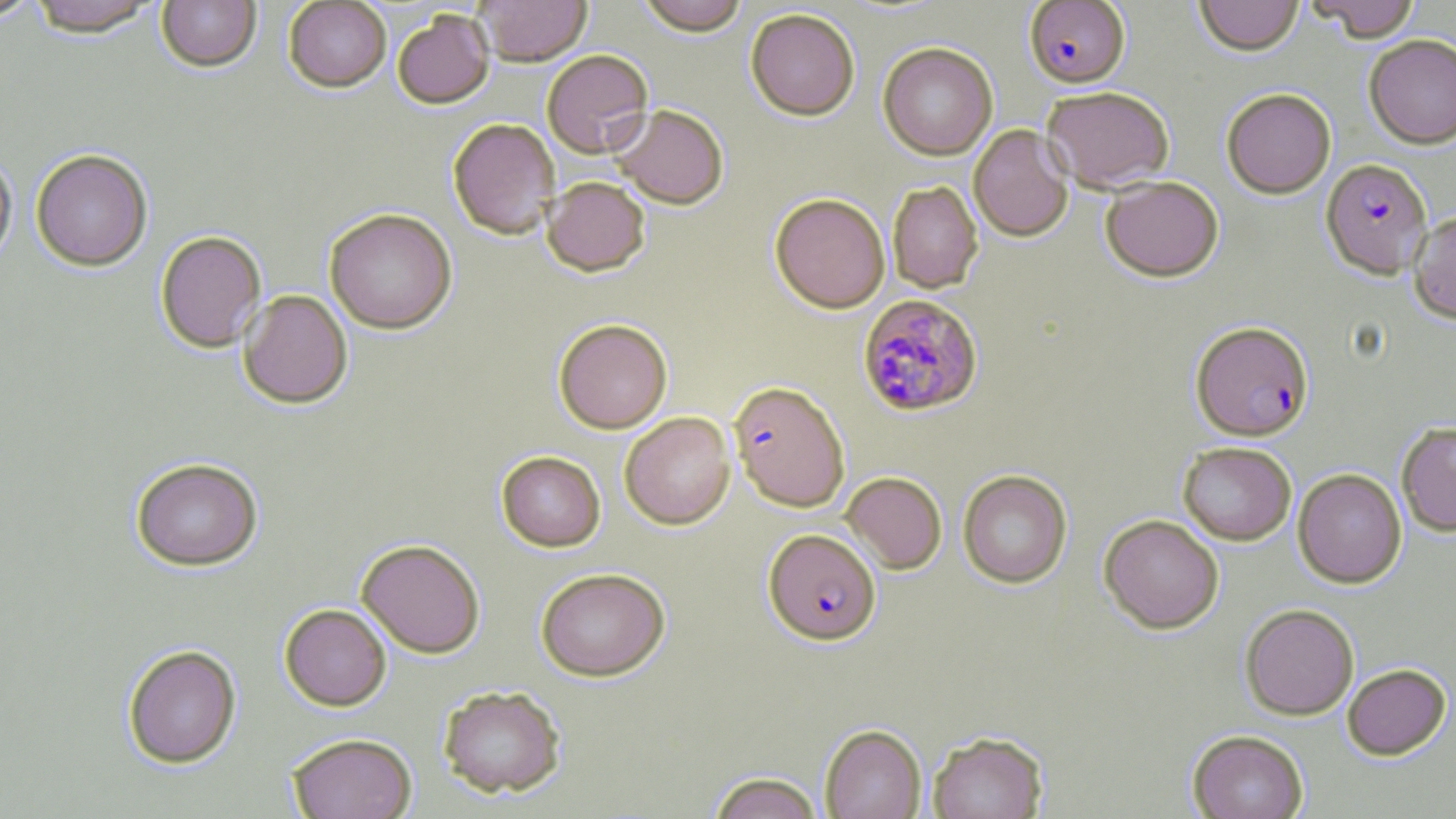
Summary:
  - Coordinate format: approximate bounding boxes as (x1,y1)-(x2,y2) corner pairs in pixels
  - Uninfected red blood cell locations: (0,0)-(44,23), (28,0)-(160,40), (156,0)-(261,75), (283,0)-(391,94), (475,0)-(592,68), (636,0)-(749,38), (1194,0)-(1304,58), (1308,0)-(1421,44), (746,10)-(860,122), (393,11)-(495,111), (1364,35)-(1456,149), (878,43)-(997,160), (542,51)-(654,160), (1042,87)-(1174,193), (1222,89)-(1336,199), (610,106)-(728,210), (448,119)-(560,240), (968,125)-(1074,242), (31,150)-(153,272), (0,151)-(17,268), (541,177)-(650,278), (1101,177)-(1224,283), (887,181)-(983,293), (770,194)-(890,313), (324,209)-(457,335), (1408,211)-(1456,323), (155,232)-(267,353), (238,291)-(352,410), (553,319)-(672,434), (620,412)-(735,530), (1396,421)-(1456,536), (1177,442)-(1296,546), (496,451)-(606,552), (130,458)-(264,573), (1293,469)-(1406,589), (958,470)-(1072,588), (841,472)-(947,574), (1099,515)-(1224,634), (356,539)-(485,658), (535,568)-(670,682), (279,604)-(392,711), (1240,604)-(1359,721), (122,645)-(242,769), (1342,665)-(1451,762), (437,685)-(566,799), (820,725)-(926,819), (927,730)-(1049,819), (1187,731)-(1308,819), (287,733)-(417,819), (707,771)-(825,819)
  - Plasmodium falciparum-infected red blood cell locations: (1024,1)-(1130,89), (1320,159)-(1433,279), (857,294)-(983,417), (1191,322)-(1313,441), (729,382)-(849,512), (763,530)-(881,646)
  - Slide-level diagnosis: Plasmodium falciparum
  - Image size: 1456×819 pixels
  - Field of view: single
  - Preparation: thin blood smear
  - Stain: May-Grünwald-Giemsa
  - Modality: light microscopy
  - Magnification: 1000x